Evaluate for parasitized red blood cells.
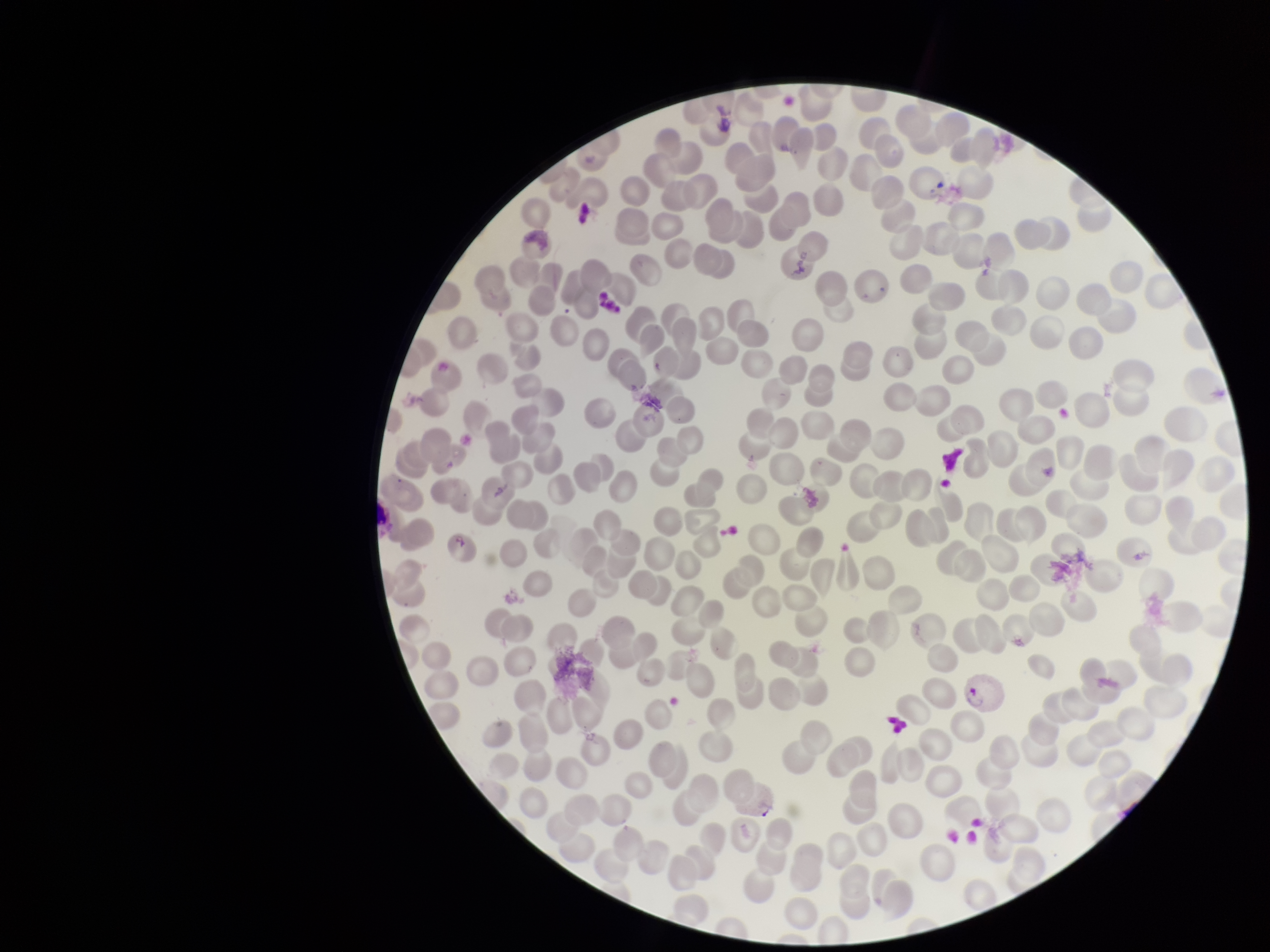
Seen.

red blood cell count = 204
capture = smartphone photograph through the microscope eyepiece
species reported for this patient = Plasmodium vivax
field of view = one from this slide
image size = 1270×952 pixels
stain = Giemsa
patient malaria status = positive
parasitized red blood cell count = 1
preparation = thin smear